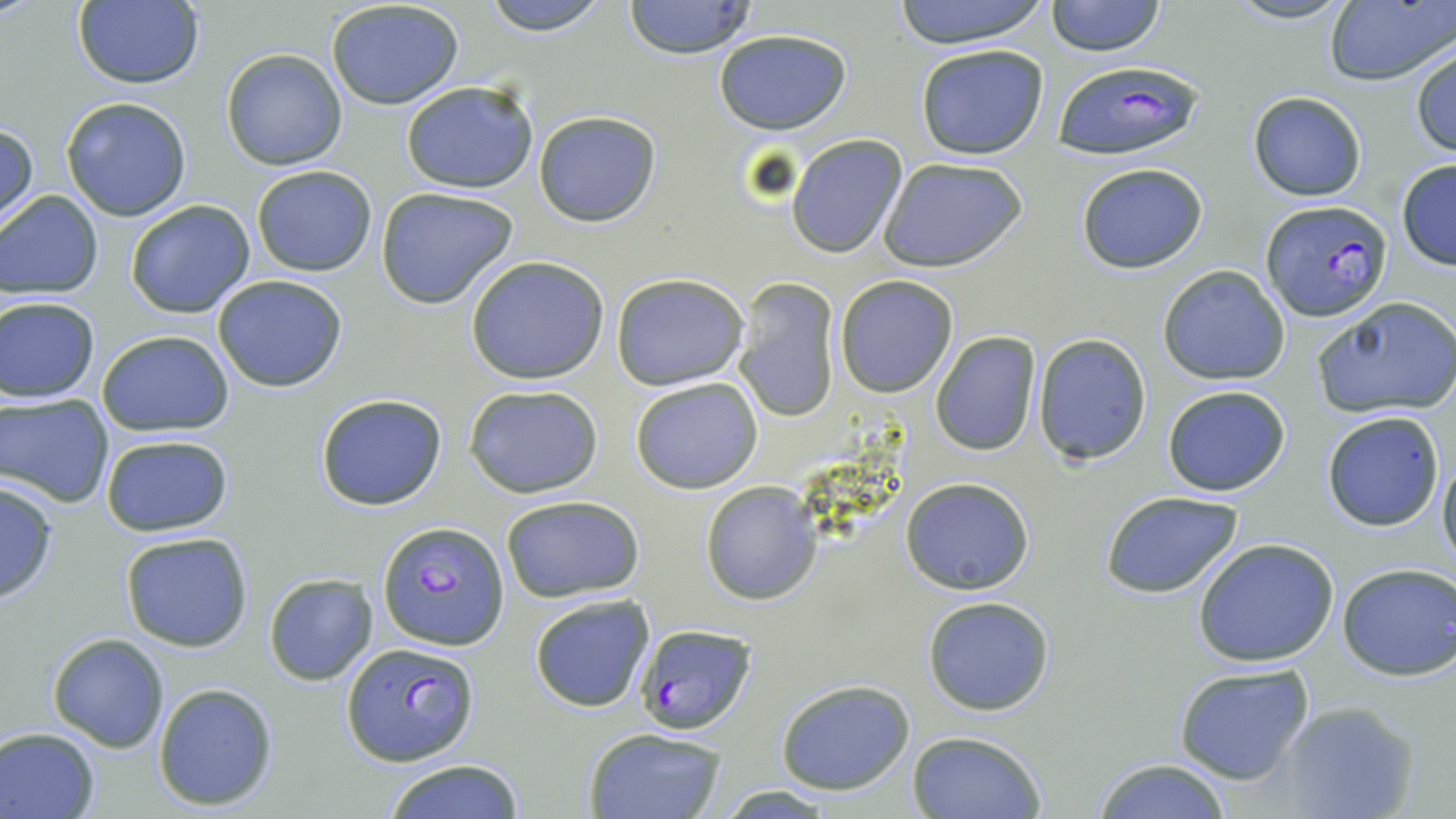

slide_level_diagnosis: Plasmodium falciparum
preparation: thin blood smear
magnification: 1000x
stain: May-Grünwald-Giemsa
image_size: 1456×819 pixels
field_of_view: one of a larger specimen
modality: light microscopy
plasmodium_falciparum_infected_red_blood_cell_locations: 'approximate bounding boxes as [x1, y1, x2, y2] in pixels: [1052, 59, 1205, 160], [1261, 200, 1393, 320], [378, 521, 509, 652], [633, 622, 759, 736], [341, 641, 479, 766]'
uninfected_red_blood_cell_locations: 'approximate bounding boxes as [x1, y1, x2, y2] in pixels: [72, 0, 204, 90], [481, 0, 612, 34], [622, 0, 759, 59], [887, 0, 1056, 48], [1046, 0, 1165, 57], [1222, 0, 1357, 26], [325, 1, 467, 111], [1322, 2, 1452, 87], [714, 29, 852, 133], [915, 43, 1049, 160], [1410, 45, 1456, 160], [220, 49, 347, 170], [400, 80, 538, 194], [1247, 92, 1367, 202], [60, 96, 192, 221], [532, 109, 662, 226], [0, 121, 38, 232], [786, 134, 908, 258], [880, 157, 1029, 273], [1394, 160, 1456, 271], [1076, 164, 1208, 275], [250, 165, 377, 277], [375, 187, 518, 308], [0, 189, 104, 301], [125, 199, 256, 318], [464, 256, 611, 386], [1158, 265, 1291, 384], [610, 274, 749, 391], [212, 275, 349, 392], [834, 276, 958, 398], [732, 278, 842, 423], [1, 295, 101, 403], [1311, 296, 1456, 418], [96, 329, 235, 436], [930, 330, 1042, 456], [1033, 333, 1151, 466], [630, 377, 764, 495], [463, 384, 604, 497], [1161, 385, 1291, 496], [1, 393, 115, 506], [314, 393, 447, 511], [1321, 410, 1445, 532], [100, 433, 234, 537], [1437, 448, 1456, 574], [901, 476, 1035, 595], [0, 480, 59, 604], [700, 480, 823, 605], [1098, 490, 1247, 599], [500, 495, 643, 603], [118, 530, 254, 653], [1192, 537, 1341, 668], [1336, 562, 1456, 681], [264, 572, 378, 686], [528, 593, 655, 713], [921, 596, 1056, 717], [47, 634, 170, 753], [1173, 664, 1315, 785], [774, 679, 916, 796], [152, 681, 279, 811], [1275, 699, 1420, 819], [0, 727, 101, 818], [581, 727, 729, 819], [905, 730, 1046, 818], [1090, 757, 1236, 819], [382, 759, 526, 819], [709, 786, 842, 816]'